Identify the preparation type.
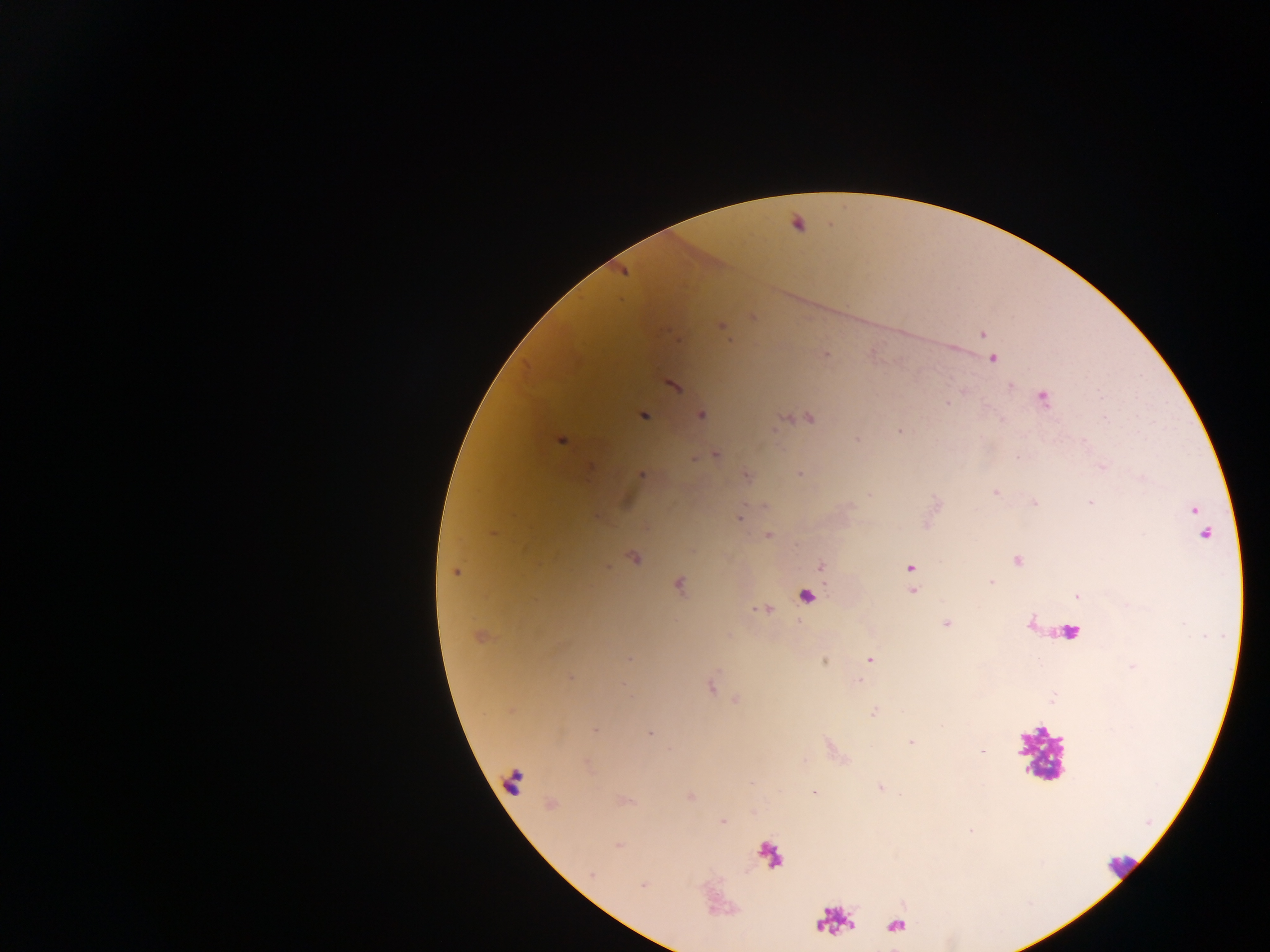
This is a thick smear.

Approximate centers as [x, y] in pixels.
Summary:
  - Malaria parasite locations: [753, 316], [721, 327], [983, 334], [678, 340], [826, 356], [993, 359], [673, 386], [1010, 386], [1043, 398], [947, 403], [643, 415], [701, 415], [1104, 417], [809, 419], [900, 431], [857, 439], [561, 441], [716, 454], [694, 459], [590, 467], [1103, 467], [800, 474], [642, 475], [746, 475], [995, 492], [1035, 503], [1090, 503], [1194, 512], [739, 517], [1204, 533], [768, 535], [634, 557], [1017, 560], [820, 565], [910, 568], [454, 572], [991, 582], [679, 586], [913, 590], [1077, 596], [763, 610], [947, 624], [478, 637], [628, 658], [869, 659], [824, 662], [570, 677], [859, 680], [711, 687], [873, 712], [595, 730], [650, 733], [911, 743], [881, 787], [814, 792], [723, 821], [970, 831], [618, 845], [592, 874]
  - Leukocyte locations: [803, 598], [1054, 631], [1040, 753], [514, 780], [1120, 865]
  - Capture: mobile-phone photograph through a microscope
  - Country: Ghana
  - Image size: 1270×952 pixels
  - Field of view: single